Assess the morphology of the red blood cells.
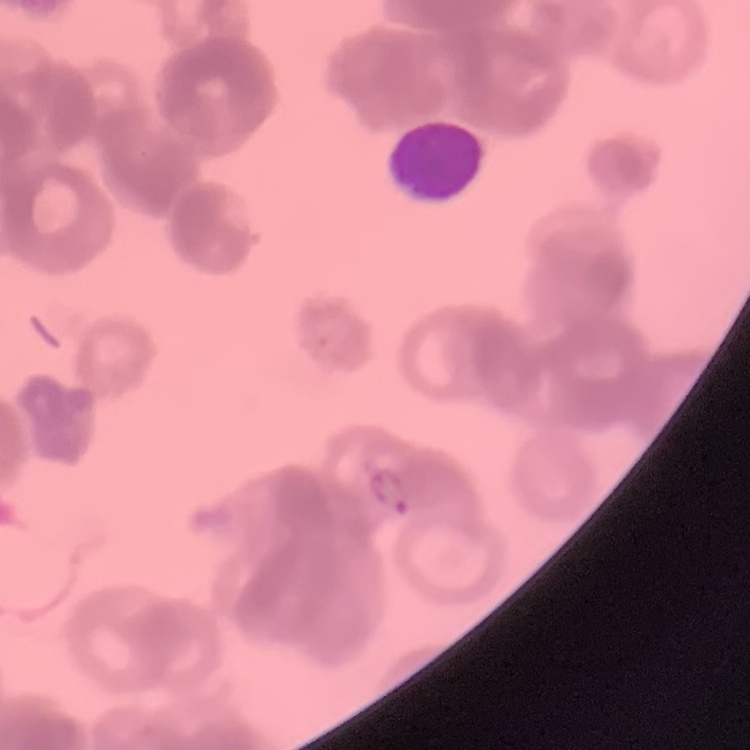

They show rouleaux formation.

preparation: thin blood smear
image_type: one tile cut from a larger photomicrograph
stain: Field's or Giemsa